Give the position of every leukocyte visible.
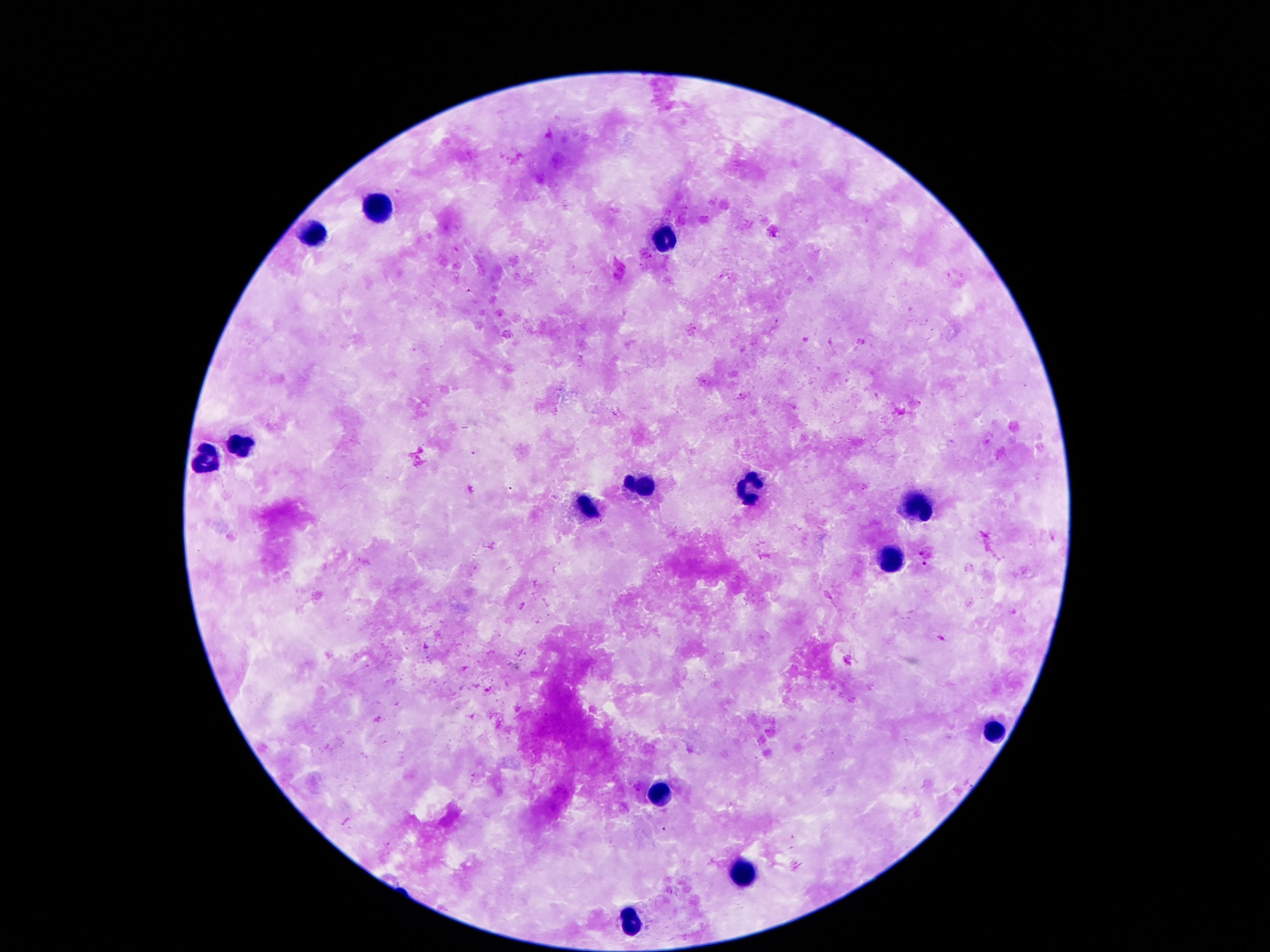

Approximate centers as {x, y} in pixels.
Leukocytes: {380, 208}, {309, 231}, {666, 241}, {241, 444}, {203, 461}, {643, 489}, {748, 494}, {920, 508}, {586, 511}, {891, 563}, {993, 732}, {661, 793}, {745, 871}, {632, 924}.

Image is 1270×952 pixels. 100x magnification. Single field of view. Giemsa-stained preparation. Thick peripheral-blood smear. Photographed through the microscope eyepiece with a smartphone camera. Patient malaria status: not infected.